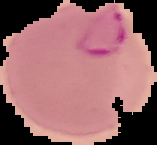
result = Plasmodium parasites detected
image type = segmented cell region on a black background
image size = 157×145 pixels
preparation = thin blood film